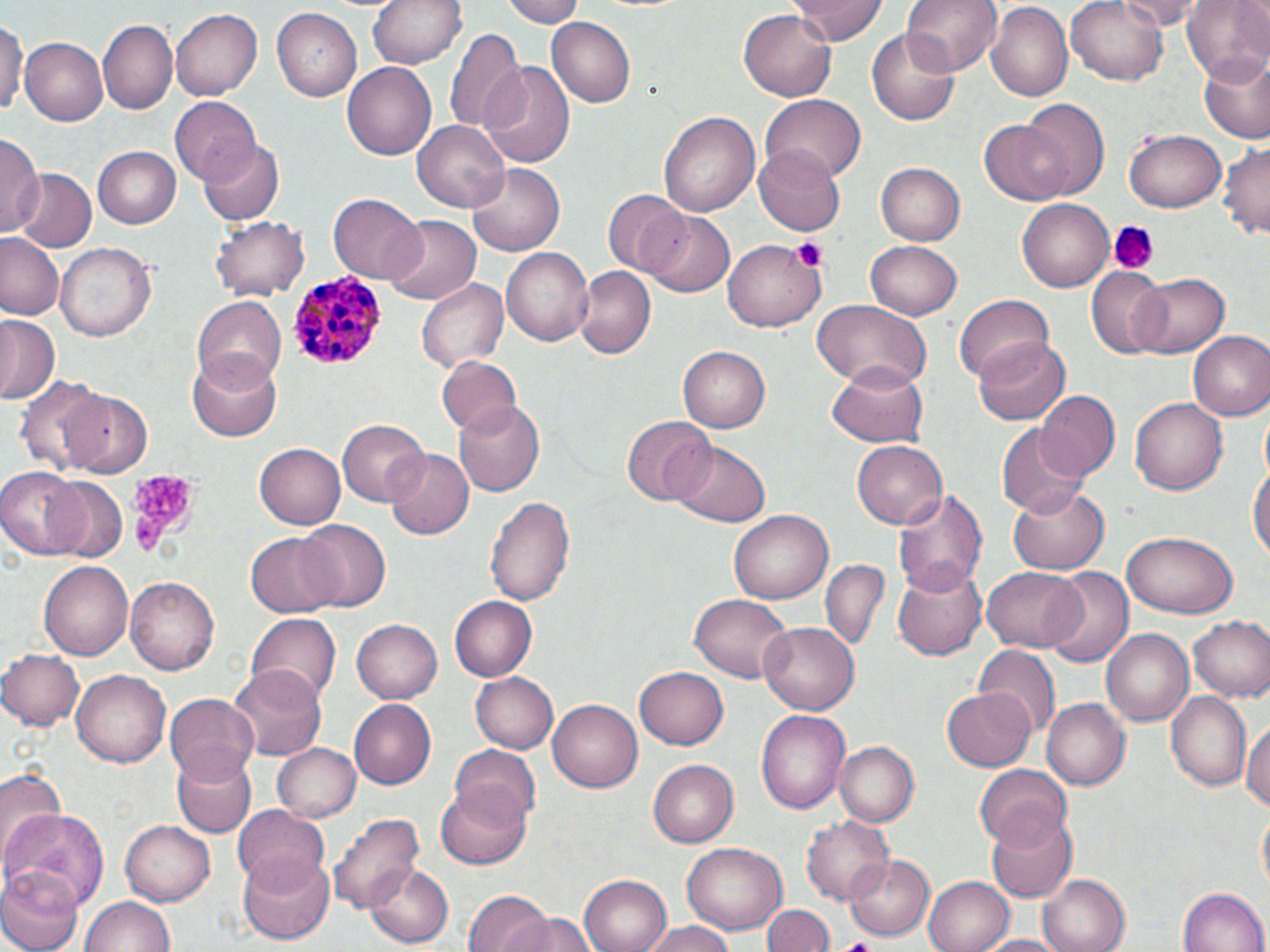
Summary:
  - Coordinate format: approximate bounding boxes as named x1/y1/x2/y2 corners in pixels
  - Plasmodium malariae-infected red blood cell locations: (x1=287, y1=268, x2=389, y2=370)
  - Platelet locations: (x1=1109, y1=223, x2=1155, y2=274), (x1=791, y1=238, x2=826, y2=272), (x1=121, y1=469, x2=202, y2=555)
  - Uninfected red blood cell locations: (x1=369, y1=0, x2=468, y2=71), (x1=501, y1=0, x2=589, y2=27), (x1=790, y1=0, x2=888, y2=45), (x1=900, y1=0, x2=1003, y2=75), (x1=1067, y1=0, x2=1170, y2=86), (x1=1121, y1=0, x2=1201, y2=28), (x1=1181, y1=1, x2=1270, y2=85), (x1=985, y1=4, x2=1071, y2=102), (x1=171, y1=7, x2=264, y2=101), (x1=273, y1=8, x2=366, y2=102), (x1=736, y1=9, x2=836, y2=102), (x1=549, y1=17, x2=638, y2=108), (x1=98, y1=19, x2=177, y2=113), (x1=0, y1=20, x2=27, y2=121), (x1=444, y1=26, x2=525, y2=135), (x1=868, y1=31, x2=960, y2=125), (x1=21, y1=38, x2=108, y2=124), (x1=1199, y1=55, x2=1270, y2=143), (x1=342, y1=57, x2=437, y2=158), (x1=482, y1=63, x2=574, y2=169), (x1=761, y1=95, x2=865, y2=182), (x1=169, y1=97, x2=260, y2=185), (x1=1018, y1=98, x2=1108, y2=198), (x1=659, y1=109, x2=759, y2=219), (x1=414, y1=119, x2=512, y2=213), (x1=979, y1=120, x2=1074, y2=206), (x1=1124, y1=129, x2=1226, y2=212), (x1=0, y1=137, x2=40, y2=236), (x1=1219, y1=139, x2=1270, y2=238), (x1=202, y1=141, x2=283, y2=226), (x1=91, y1=145, x2=179, y2=228), (x1=754, y1=148, x2=846, y2=234), (x1=877, y1=163, x2=965, y2=244), (x1=469, y1=164, x2=565, y2=255), (x1=11, y1=169, x2=96, y2=255), (x1=603, y1=189, x2=688, y2=274), (x1=328, y1=192, x2=425, y2=282), (x1=1017, y1=198, x2=1112, y2=291), (x1=400, y1=210, x2=502, y2=361), (x1=642, y1=210, x2=736, y2=298), (x1=210, y1=213, x2=311, y2=301), (x1=385, y1=215, x2=479, y2=306), (x1=0, y1=235, x2=63, y2=321), (x1=722, y1=239, x2=826, y2=333), (x1=865, y1=239, x2=962, y2=318), (x1=57, y1=243, x2=158, y2=343), (x1=500, y1=245, x2=595, y2=348), (x1=573, y1=267, x2=653, y2=359), (x1=1087, y1=270, x2=1170, y2=357), (x1=1131, y1=273, x2=1230, y2=358), (x1=417, y1=278, x2=508, y2=373), (x1=951, y1=291, x2=1054, y2=385), (x1=192, y1=295, x2=287, y2=389), (x1=811, y1=299, x2=932, y2=391), (x1=0, y1=315, x2=58, y2=405), (x1=1187, y1=331, x2=1270, y2=421), (x1=973, y1=337, x2=1072, y2=428), (x1=677, y1=345, x2=771, y2=433), (x1=187, y1=350, x2=281, y2=442), (x1=437, y1=356, x2=522, y2=438), (x1=829, y1=359, x2=930, y2=446), (x1=14, y1=377, x2=107, y2=474), (x1=61, y1=389, x2=154, y2=478), (x1=1033, y1=391, x2=1121, y2=484), (x1=453, y1=399, x2=545, y2=496), (x1=1130, y1=399, x2=1230, y2=496), (x1=622, y1=415, x2=714, y2=505), (x1=338, y1=419, x2=427, y2=505), (x1=993, y1=423, x2=1090, y2=519), (x1=671, y1=441, x2=769, y2=528), (x1=851, y1=441, x2=946, y2=528), (x1=255, y1=442, x2=347, y2=529), (x1=382, y1=450, x2=473, y2=539), (x1=1249, y1=460, x2=1270, y2=570), (x1=0, y1=467, x2=90, y2=560), (x1=43, y1=477, x2=129, y2=564), (x1=1009, y1=479, x2=1109, y2=574), (x1=893, y1=485, x2=988, y2=597), (x1=486, y1=493, x2=576, y2=610), (x1=729, y1=509, x2=834, y2=604), (x1=293, y1=518, x2=390, y2=612), (x1=247, y1=531, x2=343, y2=619), (x1=1123, y1=531, x2=1239, y2=620), (x1=820, y1=558, x2=887, y2=650), (x1=40, y1=560, x2=134, y2=662), (x1=894, y1=561, x2=987, y2=660), (x1=985, y1=565, x2=1086, y2=652), (x1=1040, y1=566, x2=1134, y2=668), (x1=127, y1=574, x2=221, y2=675), (x1=686, y1=594, x2=795, y2=683), (x1=450, y1=597, x2=537, y2=680), (x1=247, y1=614, x2=339, y2=707), (x1=1188, y1=615, x2=1269, y2=702), (x1=352, y1=618, x2=444, y2=704), (x1=760, y1=622, x2=860, y2=714), (x1=1102, y1=628, x2=1195, y2=729), (x1=977, y1=646, x2=1058, y2=731), (x1=0, y1=648, x2=85, y2=730), (x1=230, y1=662, x2=326, y2=761), (x1=634, y1=666, x2=731, y2=749), (x1=71, y1=671, x2=170, y2=768), (x1=470, y1=671, x2=558, y2=753), (x1=941, y1=685, x2=1037, y2=772), (x1=1167, y1=690, x2=1254, y2=789), (x1=165, y1=694, x2=260, y2=787), (x1=547, y1=696, x2=642, y2=789), (x1=1042, y1=697, x2=1130, y2=791), (x1=346, y1=699, x2=435, y2=790), (x1=756, y1=710, x2=849, y2=814), (x1=1241, y1=719, x2=1269, y2=817), (x1=273, y1=742, x2=363, y2=823), (x1=837, y1=742, x2=919, y2=828), (x1=451, y1=746, x2=544, y2=832), (x1=171, y1=750, x2=257, y2=836), (x1=646, y1=759, x2=738, y2=848), (x1=973, y1=764, x2=1071, y2=848), (x1=0, y1=765, x2=66, y2=858), (x1=436, y1=784, x2=531, y2=869), (x1=3, y1=807, x2=107, y2=908), (x1=233, y1=807, x2=329, y2=890), (x1=1256, y1=808, x2=1270, y2=897), (x1=328, y1=810, x2=427, y2=911), (x1=987, y1=813, x2=1078, y2=903), (x1=802, y1=814, x2=896, y2=903), (x1=120, y1=820, x2=215, y2=906), (x1=682, y1=839, x2=789, y2=934), (x1=236, y1=851, x2=337, y2=945), (x1=848, y1=853, x2=935, y2=939), (x1=1, y1=863, x2=82, y2=952), (x1=364, y1=864, x2=454, y2=946), (x1=580, y1=874, x2=673, y2=952), (x1=1040, y1=874, x2=1130, y2=952), (x1=926, y1=875, x2=1015, y2=952), (x1=1179, y1=885, x2=1268, y2=952), (x1=464, y1=892, x2=564, y2=952), (x1=81, y1=895, x2=178, y2=952), (x1=761, y1=903, x2=834, y2=952), (x1=497, y1=912, x2=601, y2=952), (x1=643, y1=924, x2=739, y2=952), (x1=977, y1=933, x2=1073, y2=951)
  - Slide-level diagnosis: Plasmodium malariae
  - Image size: 1270×952 pixels
  - Magnification: 1000x
  - Modality: light microscopy
  - Preparation: thin blood film
  - Field of view: one of a larger specimen
  - Stain: May-Grünwald-Giemsa